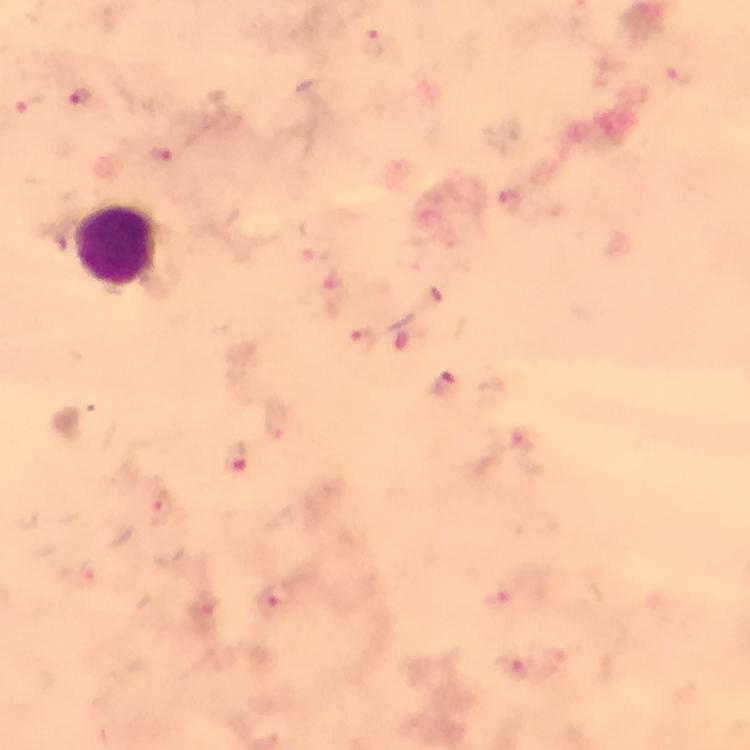
{
  "capture": "smartphone camera through the microscope",
  "immersion_oil": "used",
  "leukocyte_locations": "approximate centers as [x, y] in pixels: [118, 244]",
  "preparation": "thick blood film",
  "context": "from a malaria diagnostic workup",
  "stain": "Giemsa",
  "image_size": "750×750 pixels",
  "cropped_from": "a single field of view",
  "magnification": "100x",
  "plasmodium_parasite_locations": "approximate centers as [x, y] in pixels: [372, 44], [677, 74], [81, 96], [31, 104], [161, 153], [509, 201], [317, 251], [335, 286], [362, 339], [441, 385], [521, 441], [235, 456], [160, 508], [277, 596], [495, 602], [203, 606], [511, 666]"
}